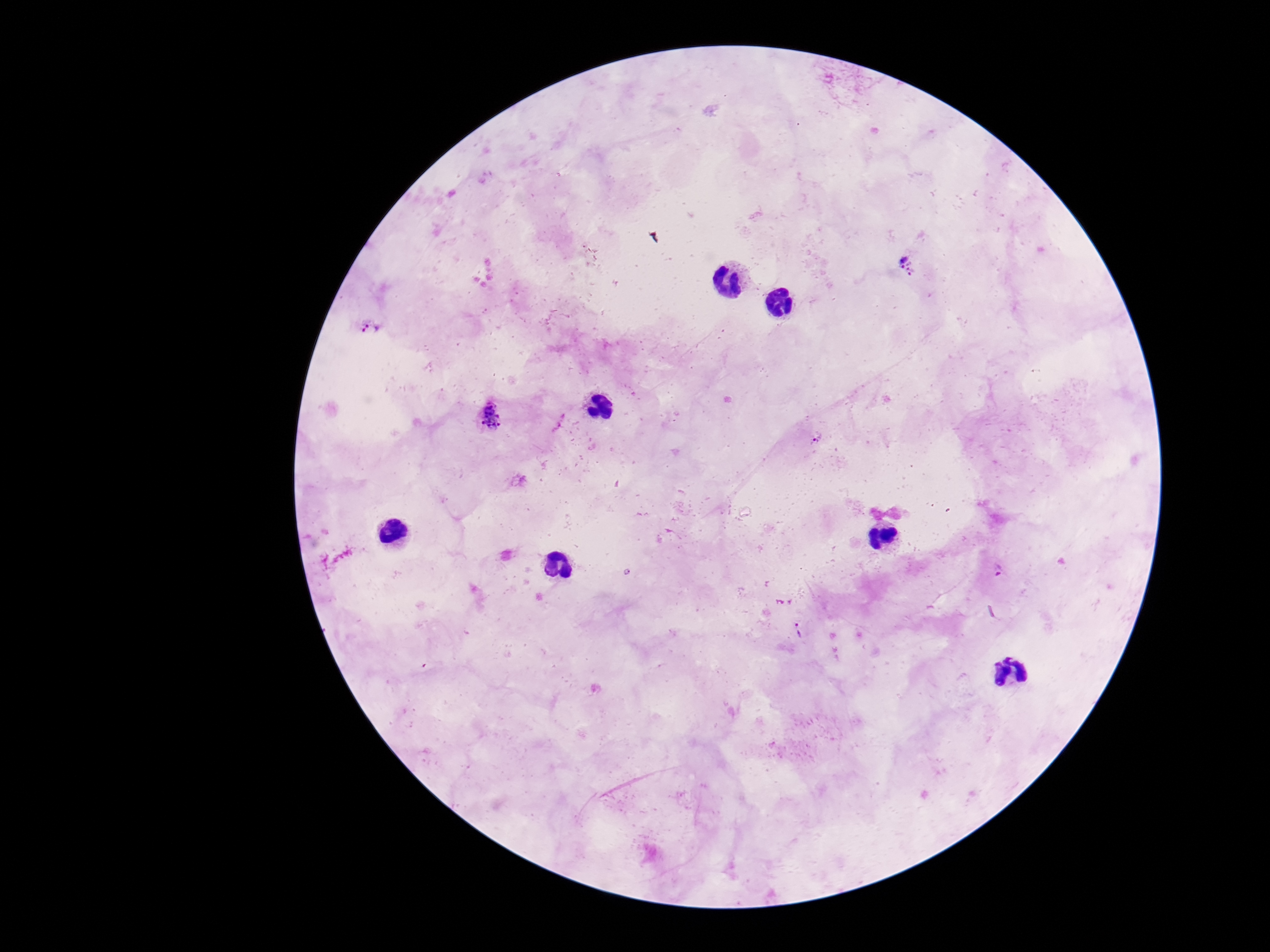

{
  "stain": "Giemsa",
  "capture": "smartphone camera through the microscope eyepiece",
  "plasmodium_parasite_locations": "approximate centers as [x, y] in pixels: [908, 265], [371, 328], [491, 419], [816, 439], [1000, 572], [799, 631]",
  "image_size": "1270×952 pixels",
  "field_of_view": "one from this slide",
  "patient_malaria_status": "positive",
  "preparation": "thick blood film",
  "magnification": "100x"
}